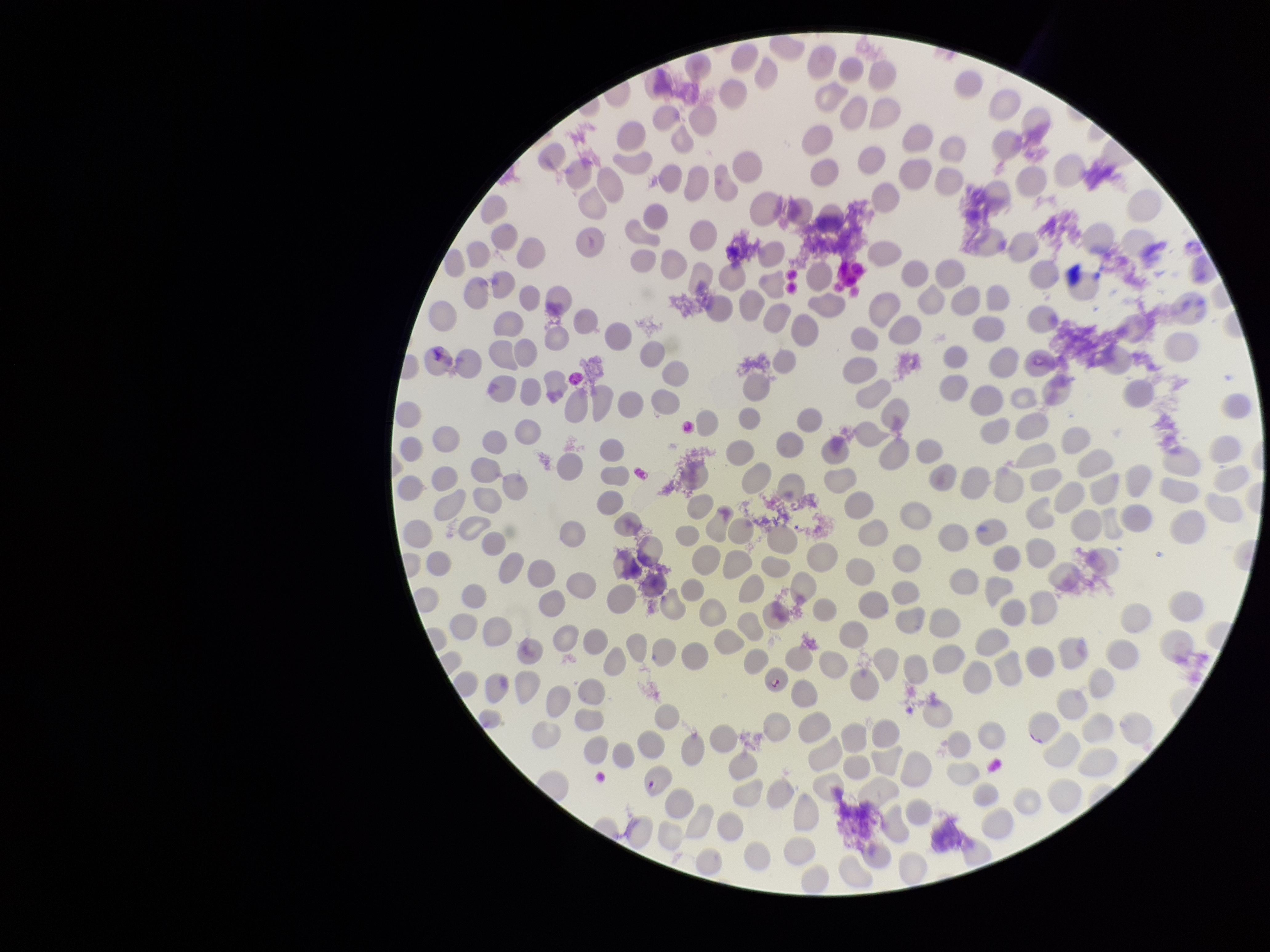

Smartphone photograph taken through the eyepiece of a microscope. Preparation: thin smear. Giemsa stain. One field from this slide. Parasitized red blood cells: detected. Parasitized red blood cell count: 2. Patient malaria status: infected. Image is 1270×952 pixels. Red blood cell count: 280. Species reported for this patient: Plasmodium falciparum.